State which parasite is depicted.
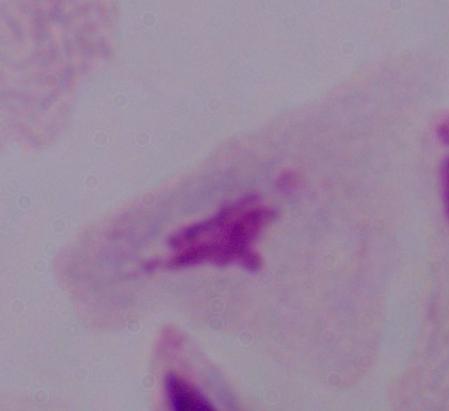
A trichomonad.

Captured at 1000x magnification. Photomicrograph.